Report the malaria status of this cell.
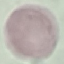
Uninfected.

stain = Giemsa
preparation = thin blood smear
capture = smartphone through the microscope eyepiece
image type = cell patch, automatically extracted from a larger field of view and resized to 64 × 64 pixels